Identify the cell.
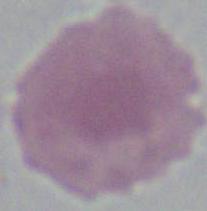

This is an erythrocyte.

modality = micrograph
magnification = 1000x